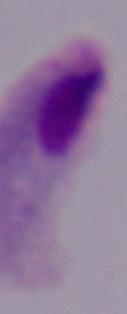
Summary:
  - Modality: photomicrograph
  - Identification: trichomonad
  - Magnification: 1000x